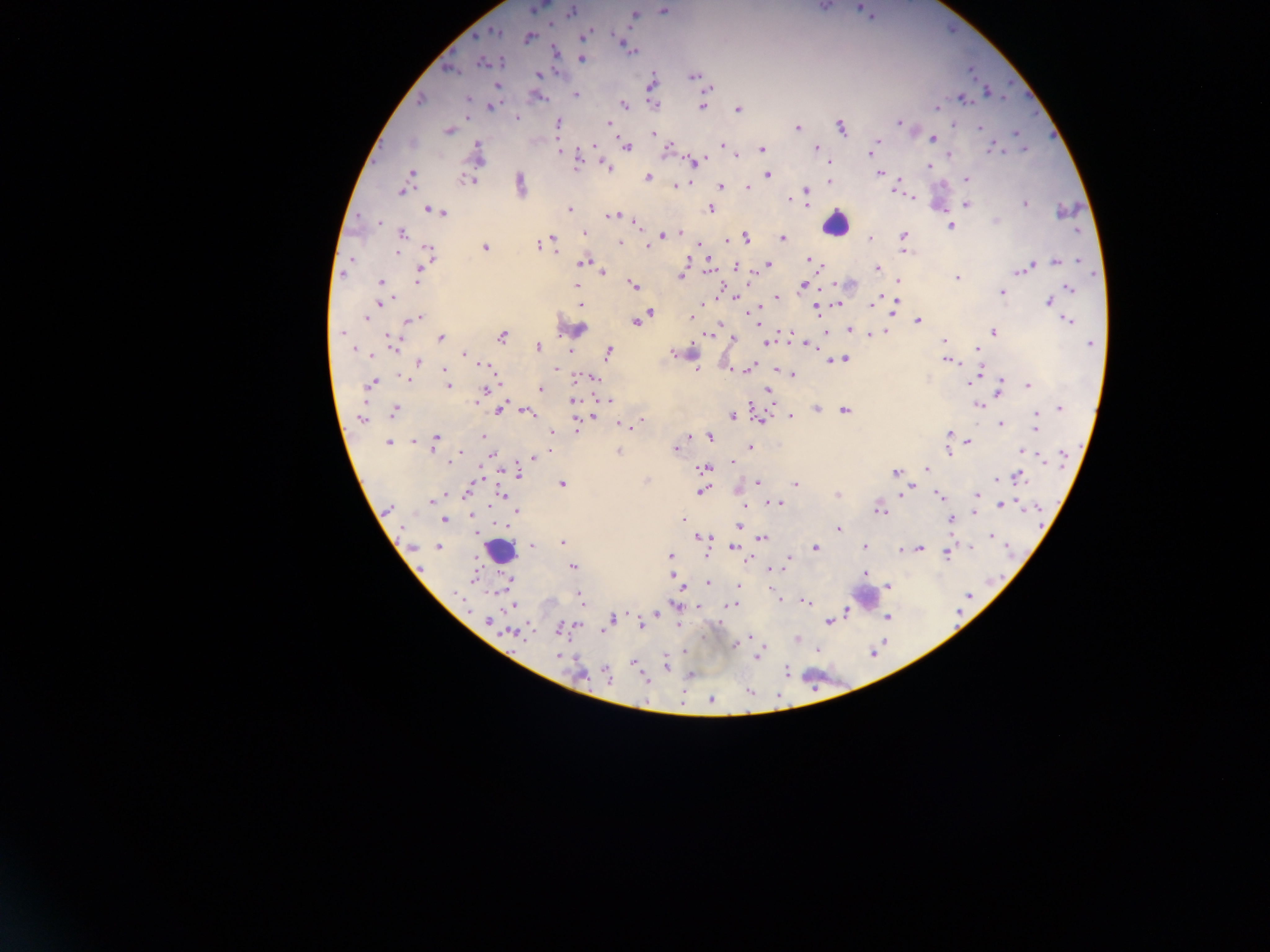
Approximate centers as x y in pixels.
Summary:
  - Leukocyte locations: 940 192; 835 225; 572 326; 696 355; 499 550; 865 597; 820 673
  - Plasmodium parasite locations: 537 7; 859 7; 662 10; 572 11; 634 15; 590 31; 495 32; 584 34; 529 37; 620 41; 628 47; 632 51; 555 52; 582 59; 483 63; 449 70; 537 74; 693 77; 651 82; 496 85; 709 88; 988 93; 576 94; 962 98; 467 99; 420 101; 654 104; 624 105; 491 106; 702 106; 936 108; 738 109; 517 118; 558 122; 609 123; 898 123; 797 127; 841 127; 980 128; 448 130; 652 134; 1016 134; 933 138; 877 141; 722 144; 593 146; 626 147; 669 147; 991 148; 1023 148; 762 149; 816 149; 560 151; 871 151; 478 153; 949 154; 736 155; 577 158; 696 160; 929 166; 607 167; 411 173; 879 173; 767 175; 647 177; 468 179; 967 180; 829 181; 683 184; 521 185; 677 185; 720 187; 748 187; 401 191; 805 191; 790 200; 966 204; 1025 204; 570 209; 710 209; 427 210; 441 213; 612 215; 996 221; 380 222; 951 226; 402 233; 584 233; 679 233; 663 235; 902 236; 745 237; 783 238; 870 239; 549 240; 727 241; 620 243; 553 244; 539 245; 647 246; 485 247; 904 251; 429 254; 808 260; 1078 260; 351 261; 687 261; 1056 261; 584 263; 768 264; 423 266; 736 267; 877 268; 709 270; 1022 270; 343 272; 603 272; 418 275; 681 276; 956 278; 899 282; 381 283; 633 285; 803 286; 577 287; 1069 288; 1001 292; 1064 292; 733 297; 777 297; 393 298; 1048 301; 379 303; 582 304; 838 304; 872 304; 816 308; 895 308; 650 312; 367 317; 417 317; 691 317; 411 319; 1067 320; 918 321; 637 322; 850 330; 341 333; 883 333; 993 333; 709 334; 871 335; 440 337; 502 337; 733 338; 944 341; 394 342; 765 342; 1090 343; 538 347; 808 347; 354 349; 978 349; 570 352; 608 352; 673 352; 368 354; 464 354; 842 359; 947 360; 418 362; 485 365; 750 368; 556 369; 444 370; 696 370; 746 370; 978 371; 792 374; 594 377; 974 377; 403 378; 970 382; 372 384; 1028 385; 448 386; 484 389; 541 389; 999 390; 769 392; 573 401; 608 401; 476 402; 979 405; 1060 408; 500 409; 815 409; 844 411; 395 412; 527 412; 1036 414; 732 416; 791 416; 591 418; 360 419; 761 420; 639 422; 1000 424; 619 425; 625 427; 1035 427; 576 428; 551 433; 949 433; 688 436; 483 437; 710 437; 436 440; 412 442; 969 442; 388 443; 749 448; 676 449; 550 450; 948 451; 1024 451; 618 452; 460 453; 492 455; 535 456; 1063 457; 451 460; 733 462; 704 468; 926 469; 518 472; 895 473; 1017 478; 476 480; 758 482; 562 483; 795 484; 702 491; 904 491; 466 492; 502 494; 837 494; 977 494; 938 496; 431 502; 777 503; 1002 505; 388 509; 879 510; 517 511; 975 512; 471 515; 444 519; 683 520; 951 520; 739 525; 838 529; 703 537; 991 537; 762 538; 562 542; 532 545; 865 546; 413 547; 438 547; 815 547; 735 548; 920 548; 901 550; 947 553; 669 556; 788 559; 573 567; 772 568; 865 573; 672 575; 508 580; 707 583; 738 585; 887 587; 581 597; 805 602; 731 605; 511 606; 847 611; 657 613; 887 617; 612 619; 488 620; 829 621; 641 625; 559 629; 604 630; 512 634; 750 636; 798 639; 735 645; 759 655; 559 656; 633 664; 666 664; 786 671; 606 674; 644 677; 711 699
  - Preparation: thick blood film
  - Country: Ghana
  - Image size: 1270×952 pixels
  - Field of view: single
  - Capture: mobile-phone photograph through a microscope